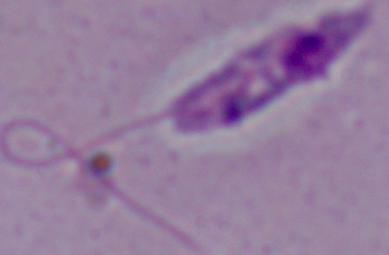

magnification = 1000x
identification = Leishmania
modality = micrograph